Report the malaria status of this cell.
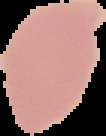
Uninfected.

preparation: thin blood smear
image_type: segmented cell region on a black background
image_size: 106×136 pixels